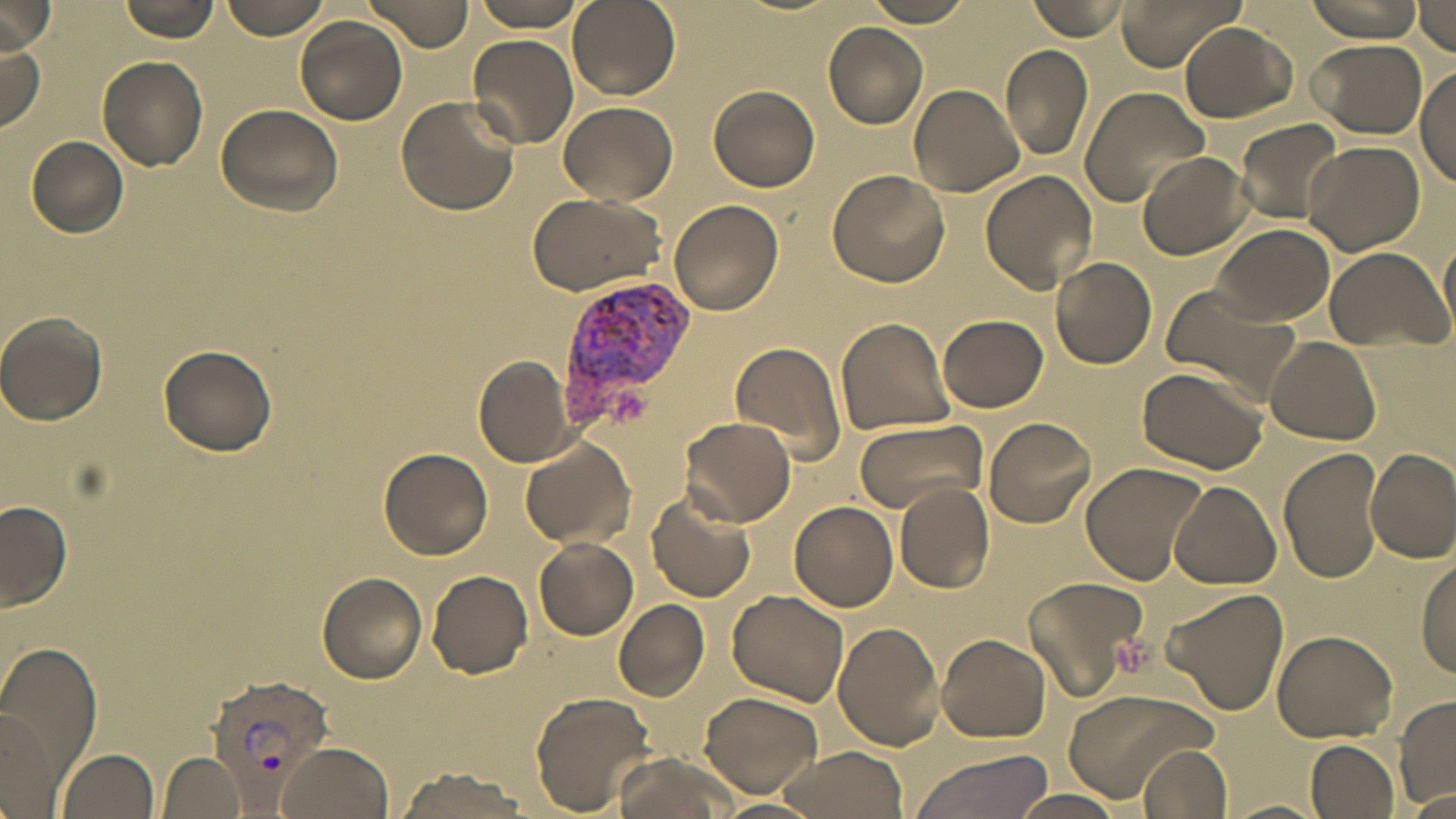 Approximate bounding boxes as [x1, y1, x2, y2] in pixels. Uninfected red blood cell locations: [118, 0, 220, 41], [220, 0, 332, 41], [360, 0, 474, 50], [464, 0, 587, 32], [567, 0, 679, 101], [1026, 0, 1132, 41], [1112, 0, 1246, 70], [1303, 0, 1426, 41], [1379, 0, 1456, 52], [866, 1, 975, 27], [1417, 2, 1455, 53], [2, 4, 55, 54], [295, 16, 408, 124], [1179, 21, 1298, 122], [823, 22, 929, 127], [466, 34, 578, 148], [1309, 39, 1428, 137], [0, 40, 46, 133], [1000, 45, 1094, 161], [97, 55, 209, 170], [1417, 69, 1456, 183], [910, 83, 1025, 197], [710, 85, 820, 192], [1078, 86, 1210, 208], [396, 95, 518, 215], [557, 101, 677, 204], [217, 104, 342, 217], [1234, 118, 1346, 225], [26, 136, 130, 238], [1305, 140, 1425, 256], [1137, 151, 1252, 259], [827, 169, 950, 289], [980, 170, 1098, 294], [525, 191, 664, 297], [667, 199, 783, 316], [1212, 222, 1335, 327], [1439, 232, 1456, 341], [1324, 246, 1452, 355], [1050, 255, 1156, 369], [1159, 283, 1303, 404], [0, 311, 108, 428], [938, 313, 1047, 413], [835, 317, 955, 436], [1264, 336, 1381, 444], [731, 340, 847, 465], [157, 344, 276, 456], [474, 355, 573, 467], [1137, 366, 1268, 476], [683, 416, 795, 526], [852, 417, 986, 515], [983, 417, 1096, 528], [520, 437, 634, 546], [663, 438, 779, 580], [380, 447, 493, 560], [1279, 448, 1384, 584], [1365, 449, 1456, 563], [1081, 462, 1207, 585], [1169, 478, 1281, 588], [894, 484, 996, 593], [647, 489, 756, 604], [1, 501, 72, 614], [790, 501, 897, 612], [534, 536, 639, 639], [1417, 554, 1456, 679], [426, 570, 533, 680], [316, 571, 427, 684], [1022, 575, 1149, 702], [1158, 586, 1289, 718], [728, 590, 850, 708], [614, 599, 710, 700], [833, 618, 944, 750], [1272, 631, 1400, 742], [935, 632, 1050, 743], [0, 647, 100, 794], [1061, 688, 1218, 803], [529, 691, 657, 813], [701, 692, 823, 797], [1394, 695, 1455, 807], [1, 707, 62, 817], [1304, 738, 1398, 818], [275, 740, 393, 819], [1138, 742, 1233, 819], [774, 746, 911, 819], [57, 749, 160, 819], [611, 750, 739, 819], [906, 750, 1056, 819], [159, 751, 246, 819], [392, 766, 530, 819], [1402, 786, 1456, 816], [1012, 788, 1125, 818], [1225, 798, 1328, 819]. Platelet locations: [1111, 629, 1156, 676]. Plasmodium vivax-infected red blood cell locations: [556, 277, 694, 421], [205, 674, 335, 794]. Slide-level diagnosis: Plasmodium vivax. Optical microscopy. Single field of view. 1000x magnification. Image is 1456×819 pixels. May-Grünwald-Giemsa stain. Thin blood film.